Locate every blood parasite and identify its species.
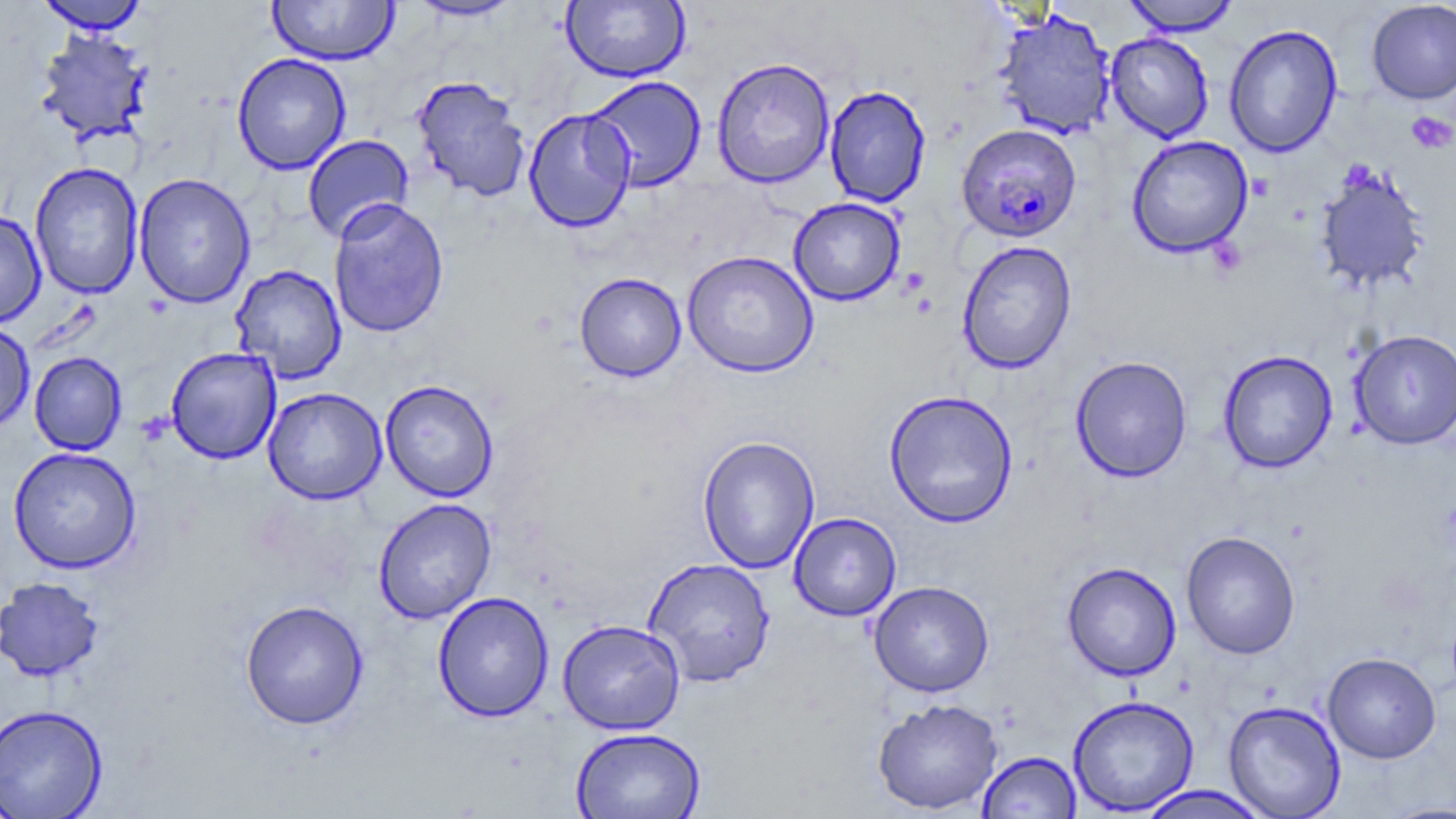

Approximate bounding boxes as (x1,y1)-(x2,y2) corner pairs in pixels.
Plasmodium falciparum-infected red blood cells: (956,123)-(1082,243).
No Plasmodium ovale, Plasmodium malariae, Plasmodium vivax, Babesia divergens, or Trypanosoma brucei observed.

Platelet locations: (1406,111)-(1455,153). Uninfected red blood cell locations: (266,0)-(400,66), (1121,0)-(1240,36), (35,1)-(149,34), (407,1)-(524,22), (561,1)-(690,83), (1366,1)-(1456,105), (994,8)-(1117,141), (1224,24)-(1343,158), (35,28)-(154,146), (1105,32)-(1214,143), (232,53)-(351,175), (712,57)-(835,189), (412,75)-(532,203), (585,75)-(707,192), (824,85)-(931,208), (523,107)-(636,233), (302,134)-(414,244), (1126,135)-(1254,258), (29,162)-(144,300), (1314,163)-(1431,293), (133,173)-(256,308), (788,197)-(906,306), (328,198)-(450,339), (0,210)-(46,328), (957,241)-(1077,374), (682,250)-(819,378), (230,264)-(347,384), (574,272)-(686,382), (0,322)-(35,435), (1349,329)-(1456,450), (165,347)-(282,465), (1218,350)-(1338,474), (29,351)-(128,455), (1070,356)-(1193,483), (380,379)-(499,502), (262,387)-(387,505), (883,389)-(1019,528), (697,435)-(820,574), (8,446)-(142,574), (374,498)-(497,624), (789,512)-(902,621), (1181,530)-(1301,659), (642,557)-(776,687), (1062,561)-(1182,681), (0,577)-(106,682), (868,580)-(994,697), (432,591)-(554,723), (240,599)-(369,730), (557,618)-(685,735), (1322,652)-(1440,763), (1067,694)-(1200,815), (871,697)-(1004,815), (1223,700)-(1346,818), (0,703)-(109,818), (570,727)-(706,819), (977,751)-(1082,818), (1134,785)-(1273,818), (1378,802)-(1456,819). Slide-level diagnosis: Plasmodium falciparum. May-Grünwald-Giemsa-stained preparation. Captured at 1000x magnification. Image is 1456×819 pixels. Thin blood smear. Light microscopy. Single field of view.